State which cell type is depicted.
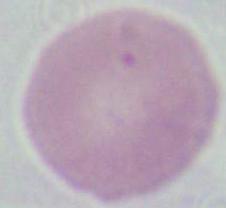

This is an erythrocyte.

modality = photomicrograph
magnification = 1000x